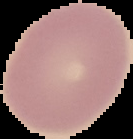

From a thin blood smear. Result: no malaria parasites detected. Image is 133×139 pixels. The area outside the segmented cell region is set to black.